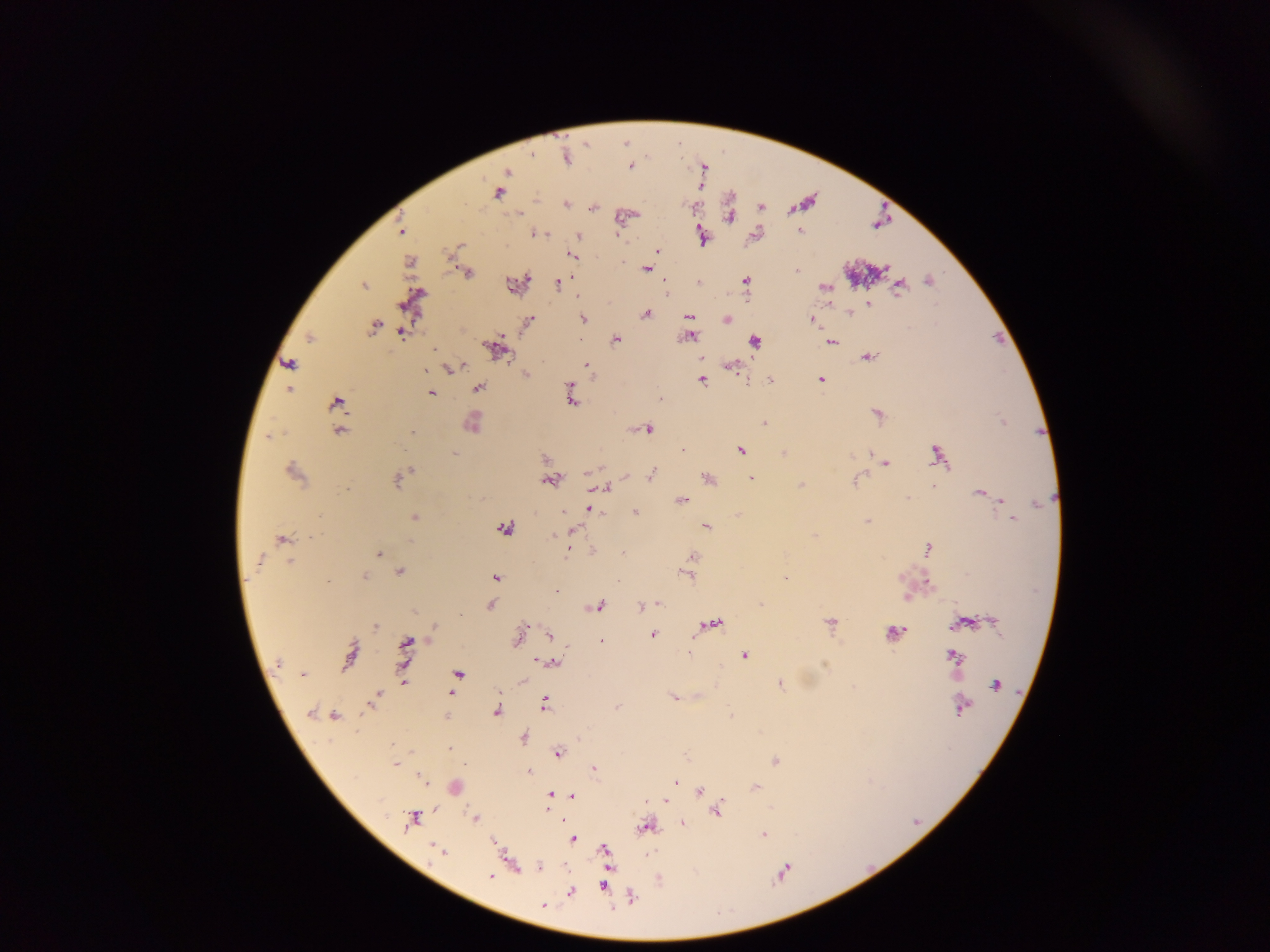

Approximate centers as {x, y} in pixels.
Summary:
  - Malaria parasite locations: {506, 171}, {499, 192}, {566, 203}, {800, 233}, {580, 236}, {656, 249}, {571, 254}, {646, 268}, {795, 271}, {666, 280}, {745, 280}, {930, 281}, {559, 283}, {897, 296}, {869, 306}, {849, 312}, {646, 313}, {687, 315}, {726, 319}, {583, 320}, {812, 321}, {374, 325}, {401, 332}, {691, 337}, {615, 338}, {486, 344}, {509, 357}, {287, 363}, {732, 366}, {451, 369}, {424, 370}, {525, 374}, {820, 377}, {771, 379}, {703, 380}, {478, 388}, {289, 390}, {432, 392}, {660, 399}, {572, 402}, {335, 403}, {766, 424}, {647, 429}, {412, 432}, {684, 450}, {740, 450}, {783, 451}, {545, 458}, {886, 464}, {948, 468}, {409, 470}, {585, 474}, {652, 474}, {626, 477}, {706, 477}, {401, 478}, {752, 479}, {550, 480}, {800, 485}, {608, 487}, {933, 488}, {978, 492}, {908, 496}, {1000, 500}, {680, 501}, {1038, 504}, {588, 510}, {636, 511}, {564, 512}, {414, 518}, {1012, 520}, {706, 526}, {503, 529}, {573, 529}, {815, 535}, {553, 536}, {282, 539}, {567, 552}, {622, 552}, {376, 553}, {692, 556}, {260, 560}, {400, 571}, {685, 574}, {364, 576}, {785, 577}, {929, 585}, {658, 603}, {759, 604}, {598, 606}, {642, 606}, {952, 627}, {523, 629}, {905, 630}, {549, 633}, {655, 634}, {518, 635}, {601, 639}, {687, 654}, {745, 656}, {536, 661}, {556, 662}, {277, 664}, {304, 673}, {524, 682}, {780, 684}, {994, 686}, {497, 696}, {674, 697}, {544, 698}, {616, 707}, {544, 709}, {367, 710}, {960, 710}, {497, 711}, {311, 712}, {334, 717}, {449, 750}, {559, 753}, {463, 765}, {395, 766}, {592, 767}, {528, 772}, {422, 778}, {425, 781}, {675, 782}, {698, 790}, {550, 794}, {573, 796}, {723, 799}, {664, 801}, {716, 812}, {413, 819}, {563, 819}, {683, 824}, {764, 836}, {575, 839}, {488, 877}, {570, 893}, {543, 905}
  - Field of view: single
  - Country: Ghana
  - Image size: 1270×952 pixels
  - Preparation: thick blood smear
  - Capture: mobile-phone photograph through a microscope